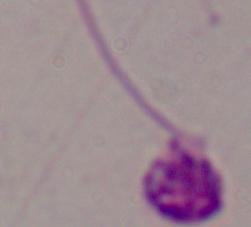

{
  "magnification": "1000x",
  "identification": "Leishmania",
  "modality": "micrograph"
}